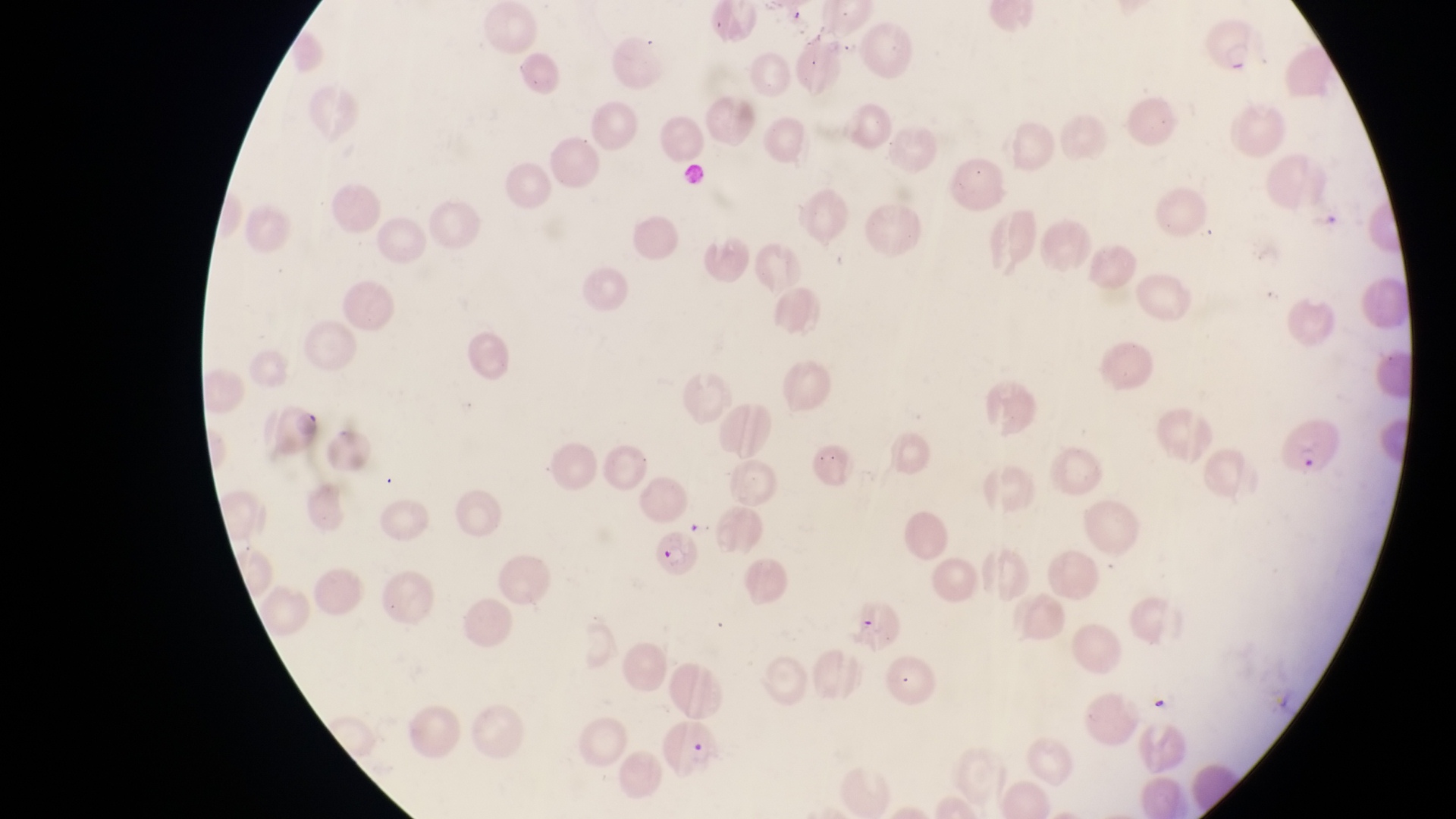 Approximate bounding boxes as [left, top, right, bottom] in pixels. Parasitised red blood cell locations: [1203, 16, 1256, 79], [268, 400, 323, 459], [1276, 416, 1345, 479], [653, 529, 700, 578]. Sample from Uganda. Photographed through the eyepiece of an Olympus CX-23 microscope with a smartphone camera. Single field of view. Image is 1456×819 pixels. Thin blood film. At a magnification of 1000x.